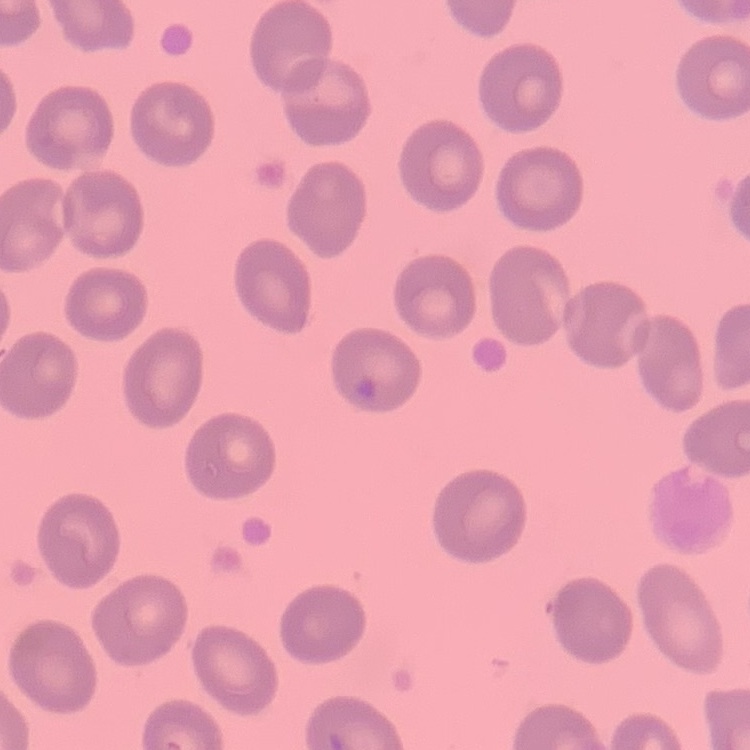

The red blood cells show no rouleaux formation. Field's or Giemsa stain. Thin peripheral smear. Square crop of a larger photomicrograph.